Give the extent of all uninfected red blood cells.
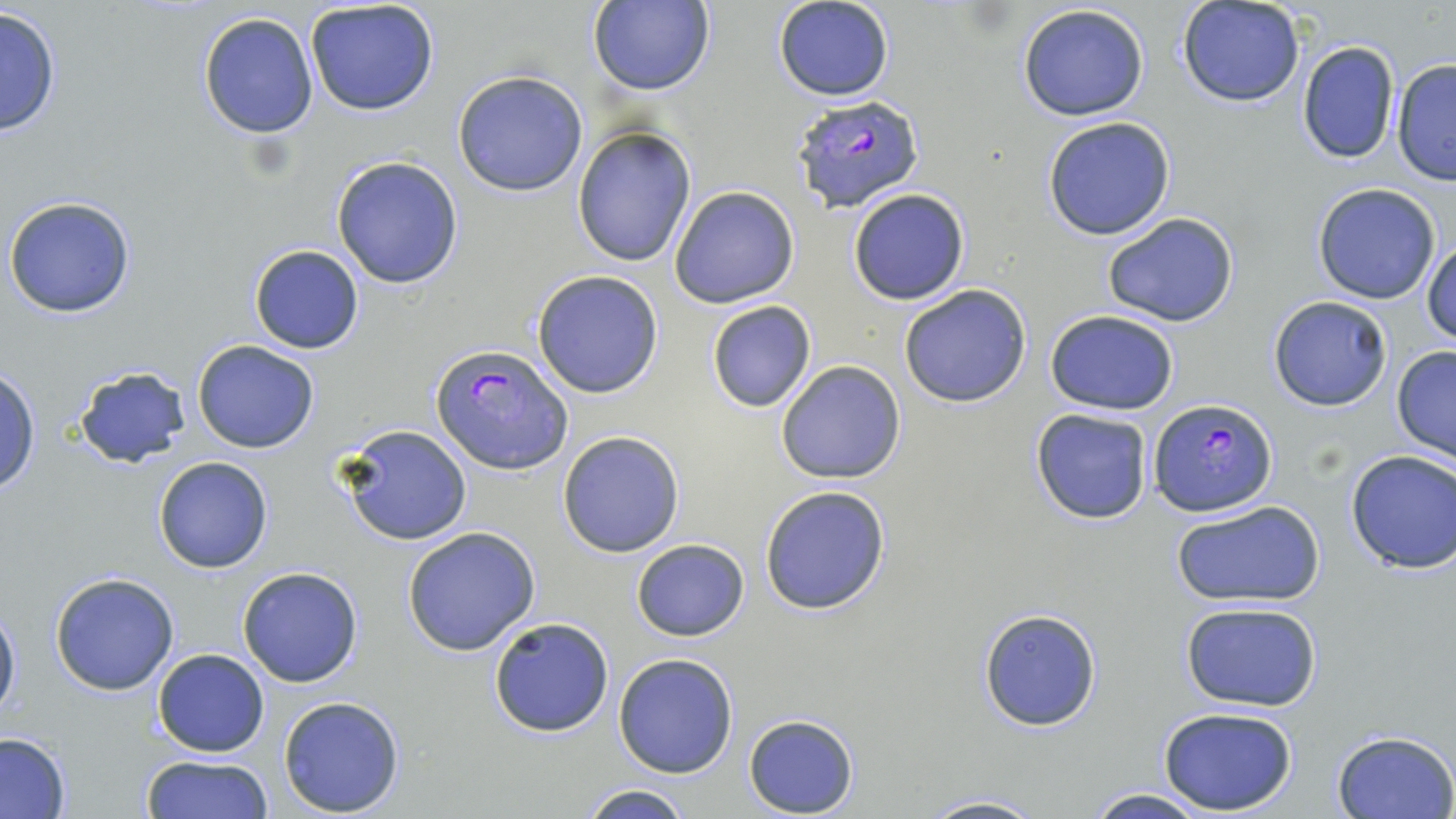
Approximate bounding boxes as (x1, y1, x2, y2) in pixels.
Uninfected red blood cells: (589, 0, 713, 96), (773, 0, 895, 102), (305, 1, 441, 116), (1178, 1, 1306, 108), (1017, 4, 1150, 121), (1, 6, 63, 137), (198, 11, 320, 140), (1295, 39, 1401, 165), (1391, 58, 1456, 185), (452, 70, 588, 196), (1041, 116, 1177, 242), (571, 127, 697, 268), (331, 155, 465, 289), (1312, 183, 1441, 303), (668, 185, 800, 310), (847, 188, 969, 305), (4, 197, 138, 318), (1100, 211, 1241, 328), (1424, 240, 1456, 345), (248, 245, 364, 353), (531, 270, 664, 398), (899, 283, 1032, 407), (1268, 296, 1393, 412), (706, 301, 816, 413), (1045, 310, 1179, 415), (193, 340, 319, 453), (1391, 348, 1456, 462), (774, 359, 908, 485), (77, 363, 191, 468), (0, 368, 40, 497), (1029, 408, 1153, 525), (336, 423, 473, 546), (557, 429, 685, 558), (1345, 450, 1456, 574), (154, 456, 273, 573), (758, 485, 892, 615), (1171, 500, 1325, 609), (403, 526, 540, 656), (630, 538, 750, 641), (237, 566, 365, 687), (49, 570, 181, 696), (1, 597, 20, 729), (1180, 603, 1322, 712), (978, 607, 1102, 732), (488, 614, 616, 739), (153, 648, 270, 756), (613, 652, 740, 779), (278, 695, 407, 816), (1155, 706, 1301, 816), (743, 714, 860, 817), (1331, 730, 1455, 819), (1, 731, 70, 817), (139, 755, 277, 817), (576, 784, 696, 819), (1079, 789, 1213, 819), (914, 793, 1047, 819).

Plasmodium falciparum-infected red blood cell locations: (791, 93, 926, 210), (431, 345, 574, 474), (1150, 398, 1276, 516). Slide-level diagnosis: Plasmodium falciparum. Optical microscopy. 1000x magnification. One field of a larger specimen. Thin blood smear. Image is 1456×819 pixels. May-Grünwald-Giemsa stain.